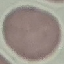
{
  "result": "negative for malaria parasites",
  "capture": "smartphone camera at the microscope eyepiece",
  "preparation": "thin smear",
  "stain": "Giemsa",
  "image_type": "cell patch, automatically extracted from a larger field of view and resized to 64 × 64 pixels"
}